Assess this cell for malaria.
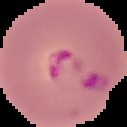
It is parasitized.

preparation = thin blood film
image size = 127×127 pixels
image type = cell region segmented out of the field of view; surrounding area masked to black